Name the parasite shown.
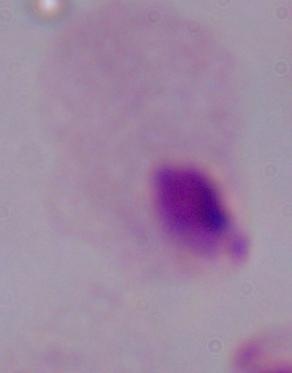
A trichomonad.

modality = micrograph
magnification = 1000x